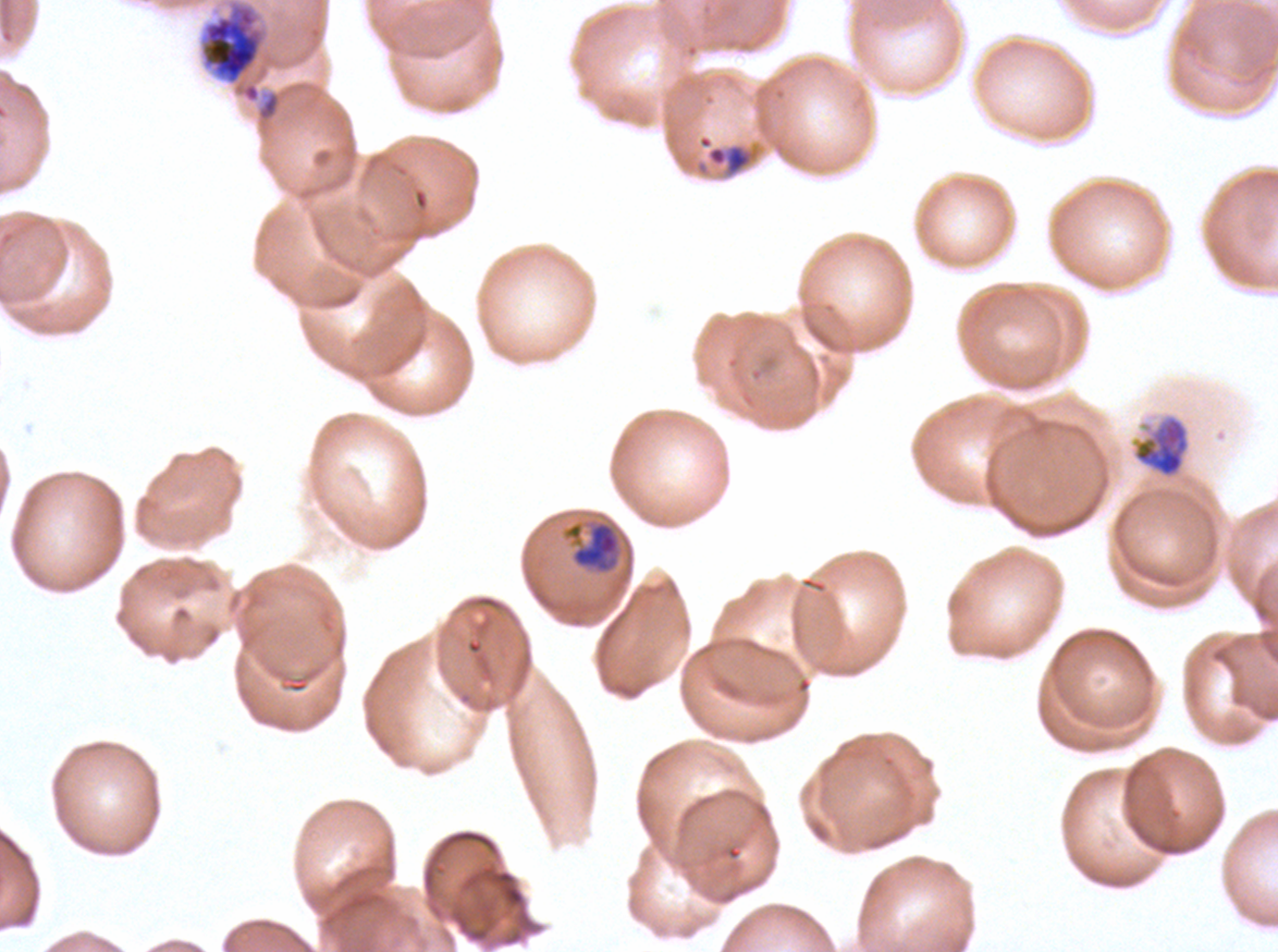
{
  "specimen": "Plasmodium falciparum cultured ex vivo for 24 to 48 hours, from a patient in The Gambia",
  "image_size": "1278×952 pixels",
  "stain": "Giemsa",
  "preparation": "thin blood film",
  "late_trophozoite_locations": "approximate bounding boxes as (x1, y1, x2, y2) in pixels: (1134, 417, 1189, 477), (560, 517, 624, 577)",
  "late_ring_early_trophozoite_locations": "approximate bounding boxes as (x1, y1, x2, y2) in pixels: (697, 134, 755, 177)",
  "early_schizont_locations": "approximate bounding boxes as (x1, y1, x2, y2) in pixels: (200, 3, 264, 85)",
  "field_of_view": "sub-image separated from a larger composite",
  "life_cycle_stages_observed": "late-ring/early-trophozoite, late trophozoite, early schizont"
}